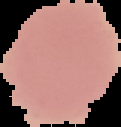

Image is 121×127 pixels. Cell region segmented out of the field of view; the surrounding area is masked to black. Malaria status: uninfected. From a thin blood film.